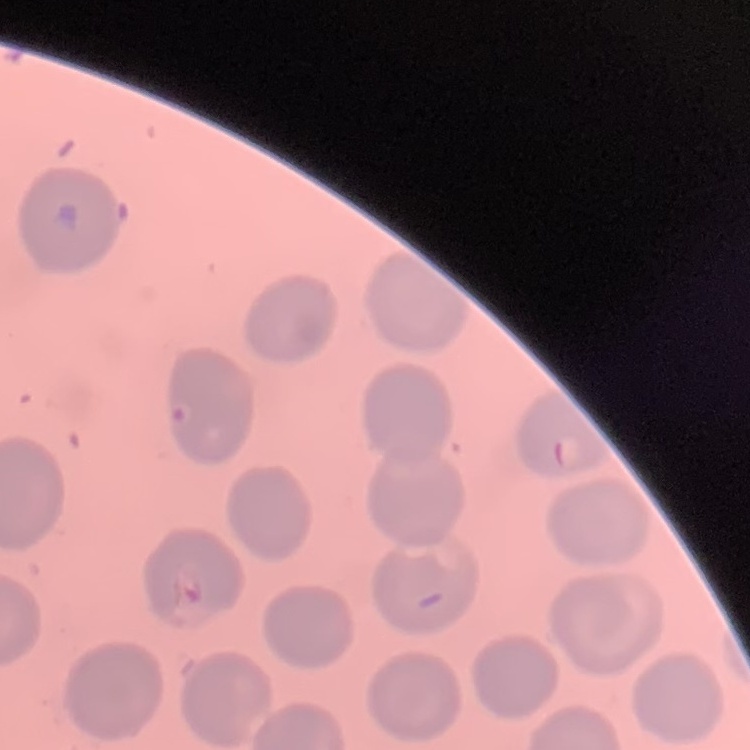 The erythrocytes show no rouleaux formation. Thin peripheral smear. Stained with either Field's or Giemsa. Square crop of a larger photomicrograph.